Assess the morphology of the red blood cells.
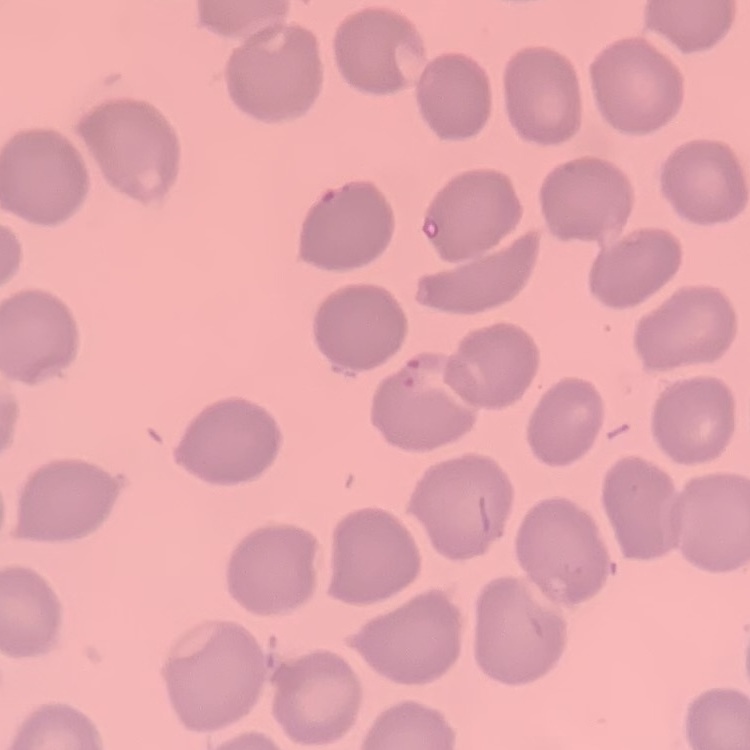
No rouleaux formation.

Summary:
  - Preparation: thin peripheral smear
  - Stain: Field's or Giemsa
  - Image type: one tile cut from a larger photomicrograph